Assess this cell for malaria.
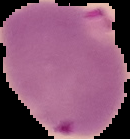

It is parasitized.

image size = 130×139 pixels
image type = cell region segmented out of the field of view; surrounding area masked to black
preparation = thin blood smear